Give the position of every Plasmodium parasite visible.
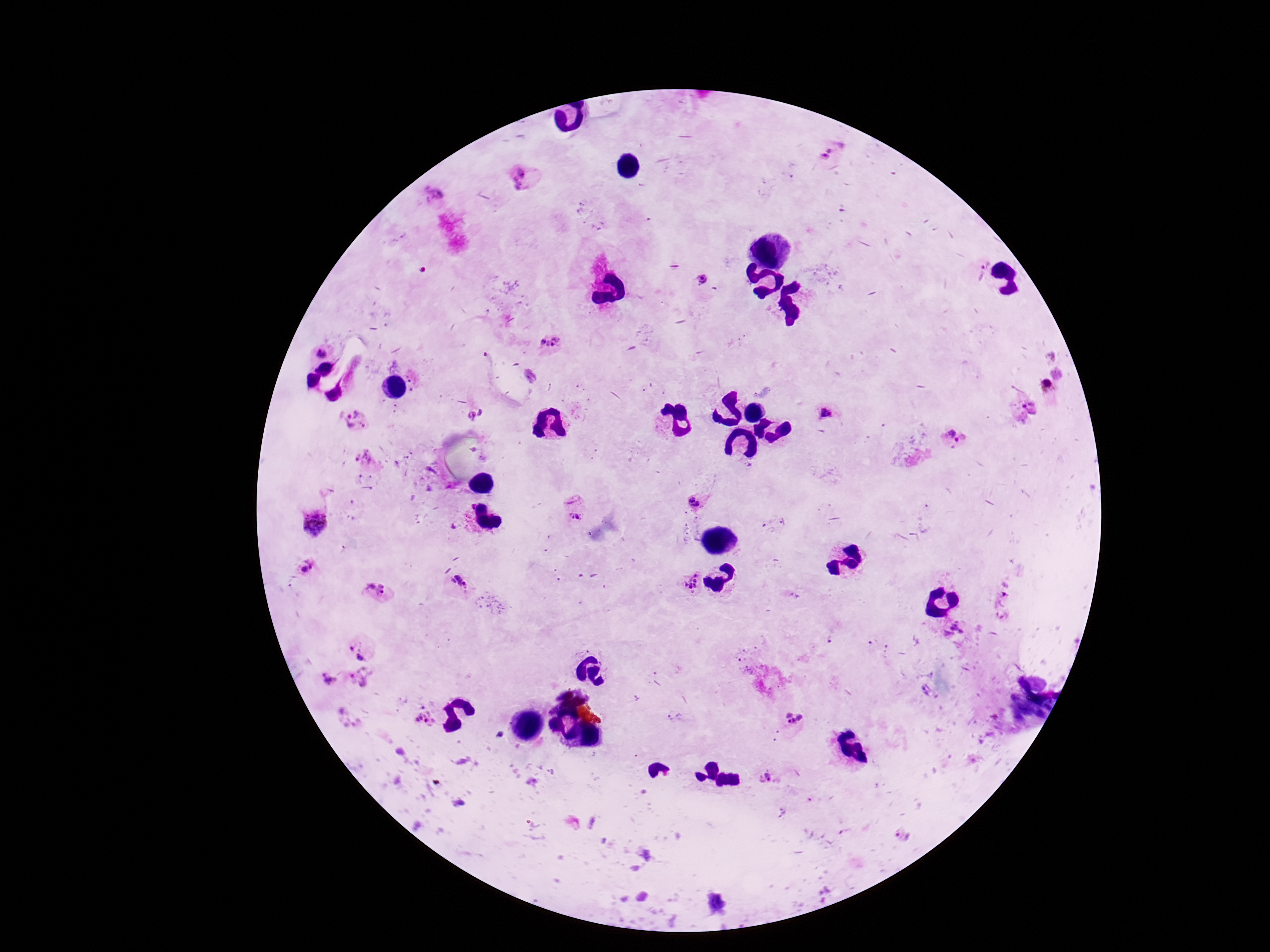

Approximate centers as {x, y} in pixels.
Plasmodium parasites: {827, 150}, {523, 179}, {981, 268}, {701, 280}, {551, 345}, {1047, 387}, {1025, 408}, {827, 412}, {482, 414}, {471, 416}, {352, 421}, {953, 438}, {362, 458}, {693, 502}, {575, 507}, {315, 523}, {307, 566}, {459, 581}, {689, 581}, {375, 590}, {954, 630}, {361, 652}, {362, 676}, {328, 677}, {675, 716}, {350, 717}, {793, 717}, {425, 719}, {769, 777}, {905, 835}.

100x magnification. Single field of view. Giemsa-stained preparation. Image is 1270×952 pixels. Thick blood smear. Photographed through the microscope eyepiece with a smartphone camera. Patient malaria status: positive.